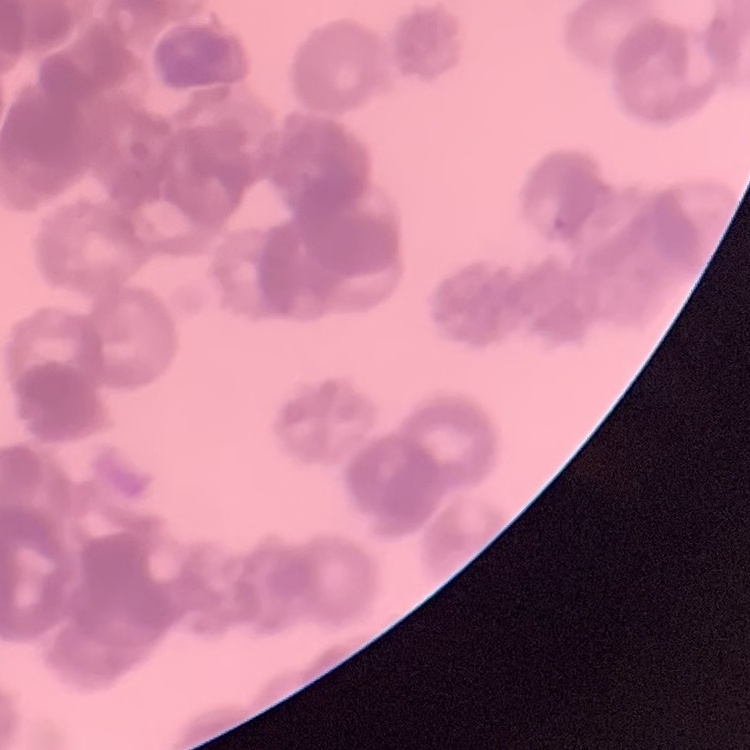
red blood cell morphology = rouleaux formation
image type = square crop of a larger photomicrograph
preparation = thin blood smear
stain = Field's or Giemsa